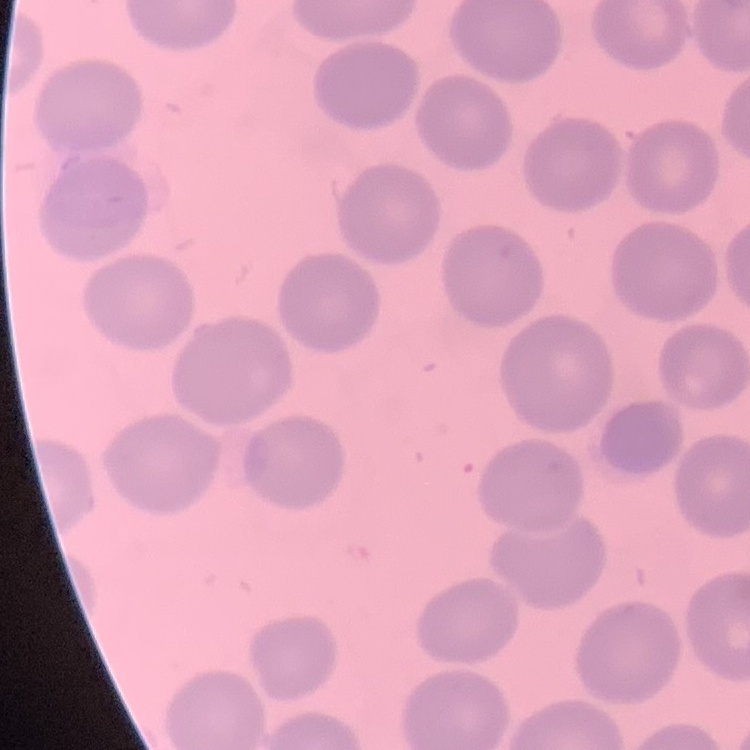

erythrocyte morphology = no rouleaux formation
preparation = thin peripheral smear
image type = one tile cut from a larger photomicrograph
stain = Field's or Giemsa